Assess this cell for malaria.
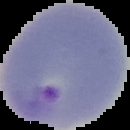
Parasitized.

Summary:
  - Image type: cell region segmented out of the field of view; surrounding area masked to black
  - Image size: 130×130 pixels
  - Preparation: thin blood film